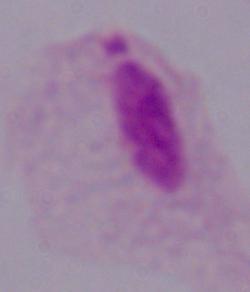 Captured at 1000x magnification. Micrograph. A trichomonad is seen.